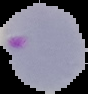

{
  "image_size": "88×94 pixels",
  "image_type": "cell region segmented out of the field of view; surrounding area masked to black",
  "result": "Plasmodium parasites identified",
  "preparation": "thin blood smear"
}